Classify this cell by malaria status.
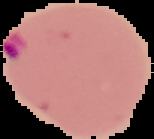
Parasitized.

Image is 154×139 pixels. Segmented cell region on a black background. From a thin blood smear.